Name the parasite shown.
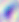
Toxoplasma gondii.

400x magnification. Photomicrograph.